State which parasite is depicted.
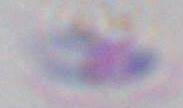

This is Toxoplasma gondii.

Summary:
  - Magnification: 1000x
  - Modality: micrograph